Identify the parasite.
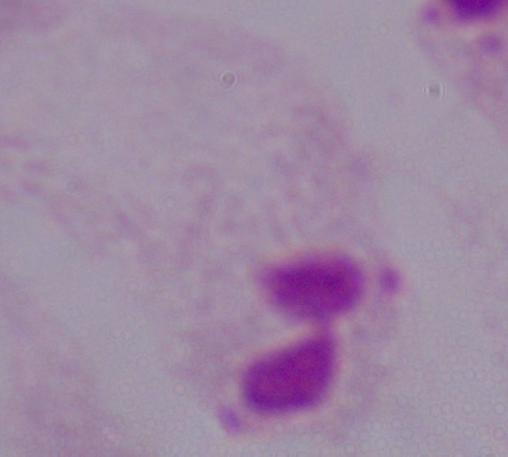

This is a trichomonad.

1000x magnification. Micrograph.